Report the malaria status of this cell.
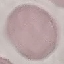
Uninfected.

Thin smear of blood. Automatically extracted cell patch, resized to 64 × 64 pixels. Giemsa stain. Acquired by smartphone through the microscope eyepiece.